Classify this cell by malaria status.
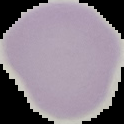
Uninfected.

Summary:
  - Image type: cell region segmented out of the field of view; surrounding area masked to black
  - Image size: 124×124 pixels
  - Preparation: thin blood smear